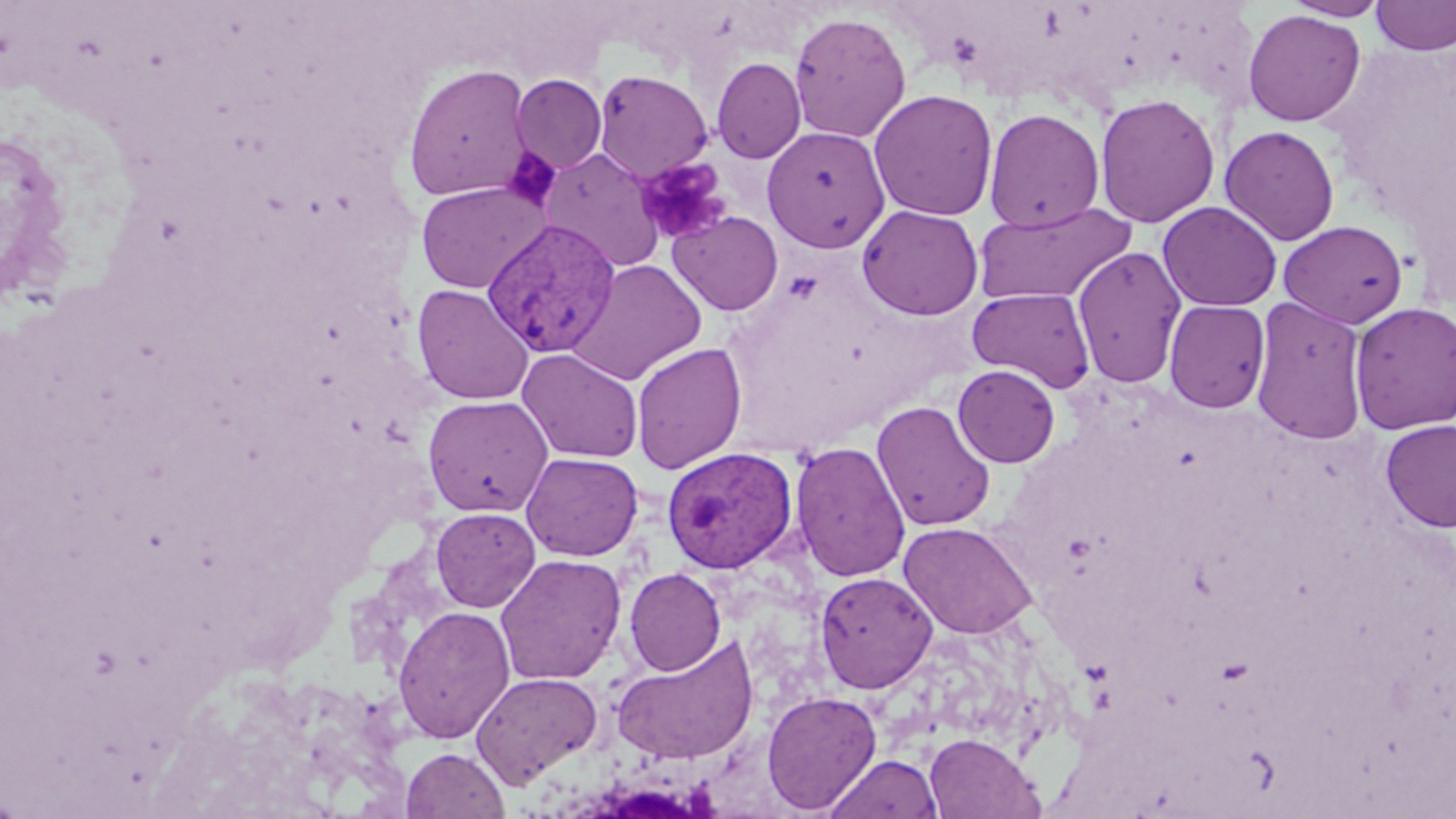

slide-level diagnosis = Plasmodium vivax
magnification = 1000x
modality = optical microscopy
platelet locations = approximate bounding boxes as named x1/y1/x2/y2 corners in pixels: (x1=501, y1=147, x2=561, y2=211), (x1=634, y1=157, x2=730, y2=244)
field of view = one of a larger specimen
stain = May-Grünwald-Giemsa
Plasmodium vivax-infected red blood cell locations = approximate bounding boxes as named x1/y1/x2/y2 corners in pixels: (x1=482, y1=217, x2=622, y2=358), (x1=662, y1=447, x2=799, y2=574)
preparation = thin blood smear
image size = 1456×819 pixels
uninfected red blood cell locations = approximate bounding boxes as named x1/y1/x2/y2 corners in pixels: (x1=1283, y1=0, x2=1390, y2=20), (x1=1371, y1=0, x2=1456, y2=56), (x1=1242, y1=9, x2=1366, y2=127), (x1=789, y1=12, x2=911, y2=143), (x1=712, y1=57, x2=806, y2=163), (x1=403, y1=64, x2=533, y2=202), (x1=593, y1=70, x2=713, y2=182), (x1=511, y1=74, x2=607, y2=174), (x1=869, y1=89, x2=998, y2=221), (x1=1095, y1=93, x2=1221, y2=228), (x1=983, y1=107, x2=1105, y2=232), (x1=762, y1=125, x2=890, y2=252), (x1=1219, y1=125, x2=1340, y2=246), (x1=540, y1=148, x2=665, y2=272), (x1=416, y1=181, x2=549, y2=293), (x1=972, y1=201, x2=1135, y2=306), (x1=1157, y1=201, x2=1282, y2=311), (x1=857, y1=205, x2=983, y2=320), (x1=668, y1=211, x2=784, y2=315), (x1=1278, y1=220, x2=1408, y2=328), (x1=1072, y1=245, x2=1187, y2=389), (x1=566, y1=258, x2=707, y2=385), (x1=412, y1=284, x2=535, y2=405), (x1=968, y1=287, x2=1096, y2=393), (x1=1250, y1=295, x2=1369, y2=444), (x1=1164, y1=299, x2=1270, y2=413), (x1=1349, y1=301, x2=1456, y2=435), (x1=631, y1=342, x2=747, y2=474), (x1=517, y1=348, x2=643, y2=463), (x1=952, y1=365, x2=1061, y2=467), (x1=422, y1=395, x2=553, y2=517), (x1=871, y1=400, x2=996, y2=531), (x1=1379, y1=419, x2=1456, y2=533), (x1=789, y1=441, x2=911, y2=583), (x1=521, y1=452, x2=643, y2=561), (x1=431, y1=507, x2=540, y2=612), (x1=898, y1=521, x2=1038, y2=639), (x1=495, y1=553, x2=627, y2=685), (x1=624, y1=568, x2=726, y2=676), (x1=814, y1=571, x2=938, y2=693), (x1=393, y1=604, x2=515, y2=743), (x1=612, y1=635, x2=760, y2=765), (x1=471, y1=672, x2=603, y2=788), (x1=761, y1=690, x2=882, y2=814), (x1=924, y1=732, x2=1042, y2=818), (x1=402, y1=747, x2=509, y2=819), (x1=826, y1=754, x2=942, y2=818)